Report the malaria status of this cell.
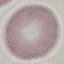
Uninfected.

Summary:
  - Preparation: thin blood film
  - Capture: smartphone camera at the microscope eyepiece
  - Image type: automatically extracted cell patch, resized to 64 × 64 pixels
  - Stain: Giemsa